Classify this cell by malaria status.
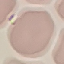
It is uninfected.

image type = automatically extracted cell patch, resized to 64 × 64 pixels
stain = Giemsa
preparation = thin smear
capture = smartphone through the microscope eyepiece